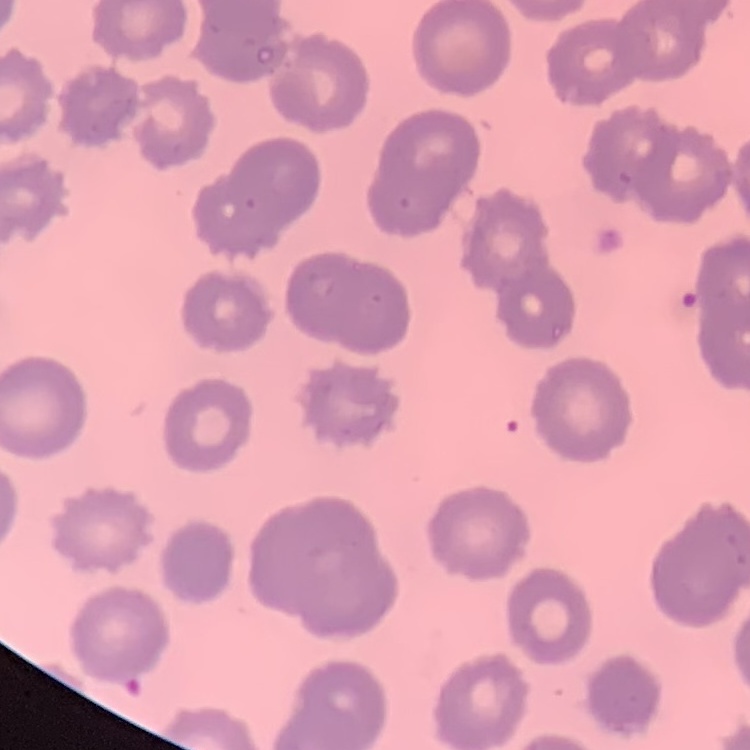

red blood cell morphology = no rouleaux formation
image type = square crop of a larger photomicrograph
preparation = thin peripheral smear
stain = Field's or Giemsa